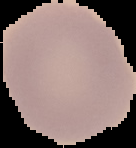

result = no malaria parasites detected
image size = 136×148 pixels
image type = segmented cell region with the area outside set to black
preparation = thin blood smear